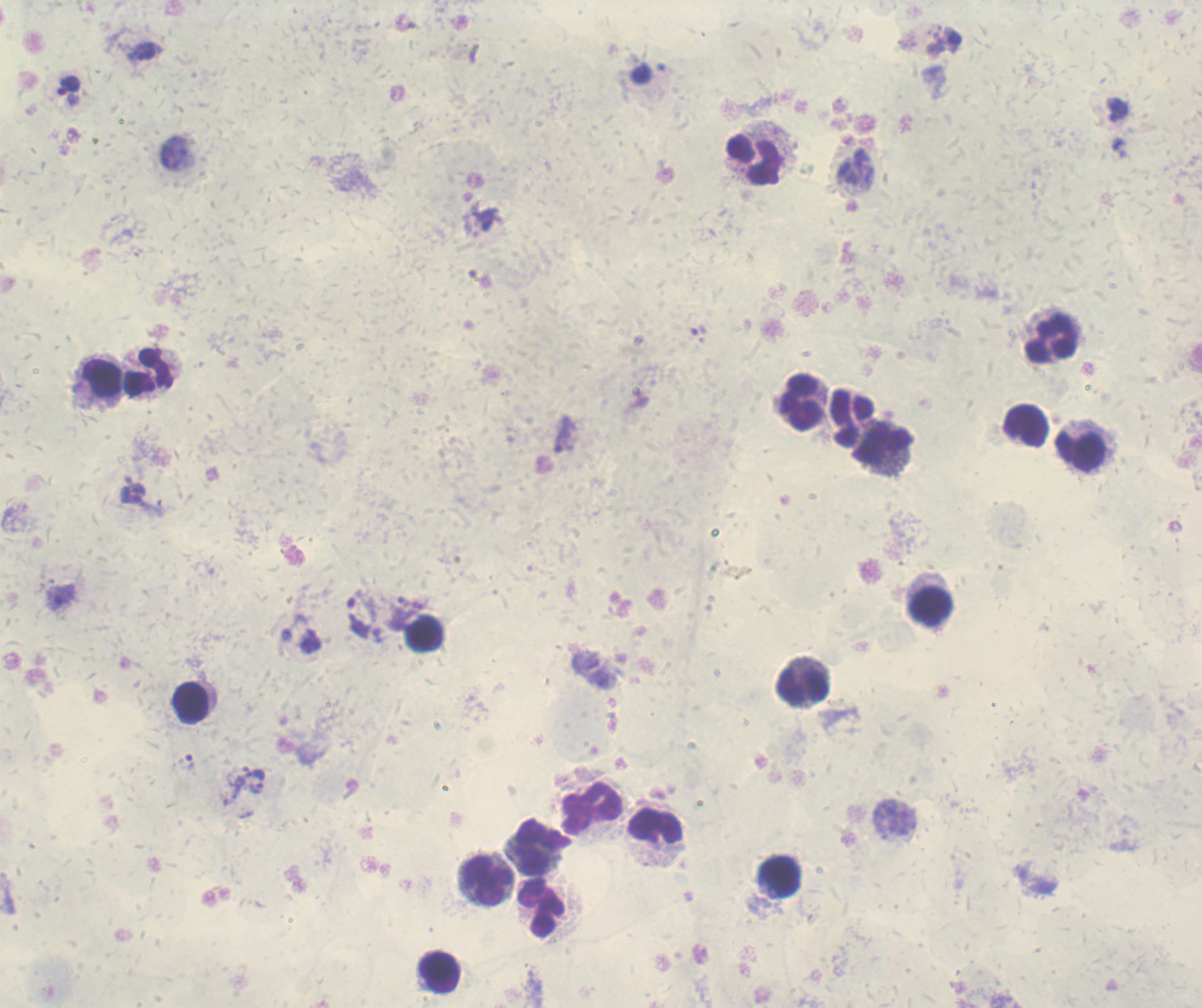
Approximate centers as [x, y] in pixels.
Summary:
  - Trophozoite locations: [405, 23], [145, 51], [68, 85], [177, 154], [480, 279], [698, 334], [132, 494], [60, 596], [402, 601], [420, 605], [360, 613], [604, 680], [185, 763], [254, 772], [258, 789], [896, 819]
  - Leukocyte locations: [755, 159], [1053, 338], [149, 373], [102, 378], [800, 402], [850, 417], [1026, 425], [883, 443], [1080, 450], [930, 608], [423, 634], [802, 686], [191, 703], [591, 808], [657, 826], [543, 847], [778, 876], [488, 880], [542, 907], [439, 971]
  - Magnification: 100x
  - Result: positive for Plasmodium parasites
  - Coloration quality: good
  - Background quality: unsatisfactory
  - Stain: Romanowsky
  - Image size: 1202×1008 pixels
  - Context: previously used in a real diagnosis
  - Preparation: thick smear of blood
  - Field of view: one from this slide